Report the malaria status of this cell.
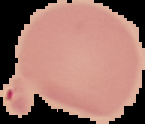

It is uninfected.

Image is 145×124 pixels. From a thin blood smear. Cell region segmented out of the field of view; the surrounding area is masked to black.